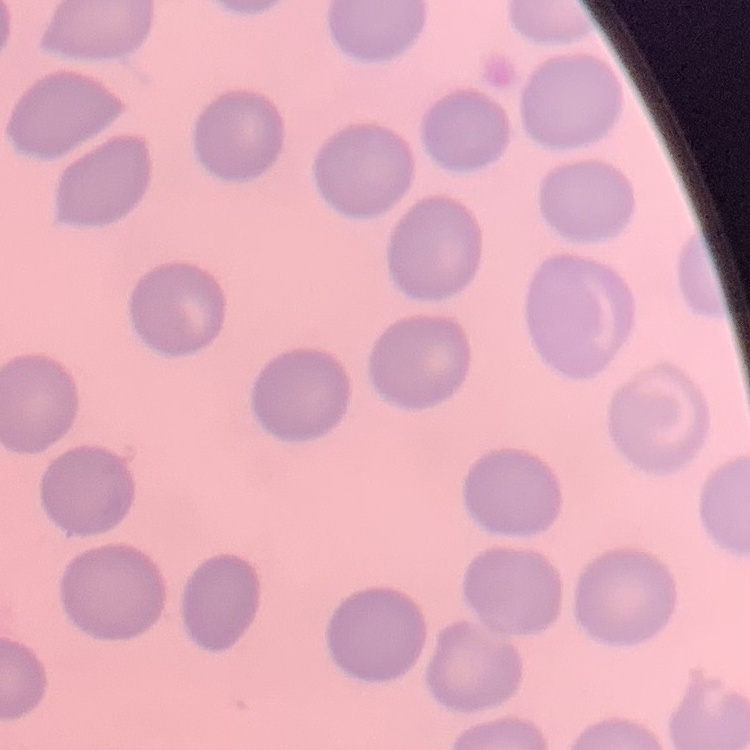
erythrocyte morphology = no rouleaux formation
image type = one tile cut from a larger photomicrograph
stain = Field's or Giemsa
preparation = thin blood smear